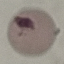
Malaria status: uninfected. Giemsa-stained preparation. Thin blood smear. Photographed with a smartphone camera at the microscope eyepiece. Automatically extracted cell patch, resized to 64 × 64 pixels.